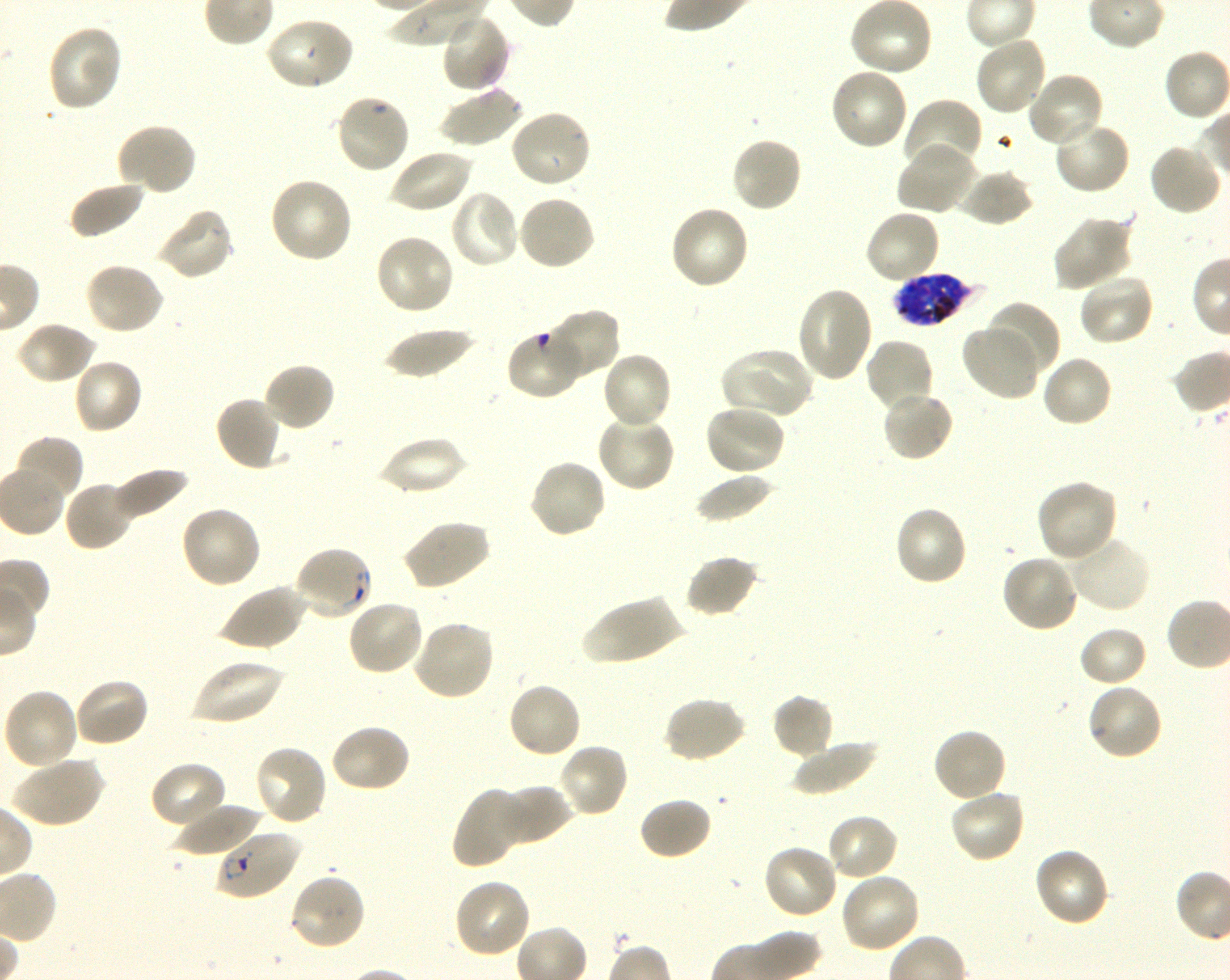
Approximate bounding boxes as (x1, y1, x2, y2) in pixels. Not every red blood cell is marked. A life-cycle stage — or a range of stages, where the recorded stages span more than one — follows each staged infected red blood cell. Locations of infected red blood cells: (889, 273, 984, 328) late trophozoite to late schizont; (215, 829, 301, 900) ring. Locations of red blood cells of indeterminate infection status: (505, 327, 583, 401), (292, 544, 375, 621). Locations of uninfected red blood cells: (440, 13, 512, 94), (265, 16, 356, 92), (46, 23, 123, 113), (973, 34, 1048, 116), (829, 67, 909, 152), (1026, 72, 1104, 151), (440, 85, 524, 148), (333, 93, 411, 175), (902, 98, 982, 173), (508, 109, 593, 190), (1053, 119, 1132, 196), (115, 123, 198, 197), (730, 135, 804, 214), (897, 142, 979, 216), (1148, 142, 1222, 217), (388, 148, 474, 215), (959, 169, 1036, 227), (268, 177, 354, 265), (68, 180, 146, 240), (448, 189, 522, 270), (516, 194, 596, 272), (668, 204, 751, 291), (154, 207, 235, 281), (864, 209, 941, 285), (1052, 214, 1135, 291), (373, 232, 456, 316), (83, 261, 164, 336), (1078, 272, 1155, 347), (796, 286, 875, 383), (985, 300, 1062, 377), (542, 308, 621, 381), (15, 321, 97, 385), (960, 326, 1038, 401), (382, 327, 477, 379), (864, 338, 935, 415), (718, 346, 812, 420), (601, 351, 674, 431), (1040, 354, 1114, 429), (72, 358, 143, 435), (262, 362, 336, 432), (880, 389, 956, 462), (214, 396, 285, 472), (703, 404, 786, 477), (595, 414, 676, 494), (376, 435, 467, 496), (13, 436, 84, 503), (527, 457, 607, 539), (110, 467, 190, 523), (695, 471, 774, 524), (1035, 478, 1118, 564), (63, 480, 137, 552), (179, 505, 261, 590), (893, 505, 969, 587), (400, 519, 490, 591), (1070, 534, 1152, 613), (1000, 553, 1081, 633), (684, 554, 761, 619), (216, 583, 305, 652), (579, 596, 687, 665), (346, 597, 426, 676), (411, 620, 496, 701), (1078, 626, 1149, 688), (190, 658, 283, 727), (73, 676, 150, 748), (506, 680, 583, 760), (1086, 681, 1164, 762), (2, 688, 80, 771), (771, 692, 836, 760), (661, 696, 746, 764), (328, 723, 412, 794), (932, 727, 1007, 804), (791, 738, 878, 796), (557, 742, 629, 819), (252, 743, 328, 828), (12, 756, 105, 828), (149, 760, 228, 829), (497, 784, 573, 846), (451, 787, 530, 869), (948, 787, 1027, 864), (639, 795, 712, 861), (175, 803, 261, 861), (825, 814, 899, 883), (761, 843, 839, 921), (1033, 846, 1112, 928), (288, 872, 367, 952), (838, 872, 920, 955), (452, 878, 533, 959). Plasmodium falciparum strain 3D7 in shaking in-vitro culture. Oil immersion, 100x objective (numerical aperture 1.30). Blood group of the donor: O+. Single field of view. Giemsa-stained preparation. Thin blood film. Image is 1230×980 pixels.